Identify the cell.
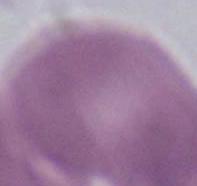
This is an erythrocyte.

Summary:
  - Magnification: 1000x
  - Modality: photomicrograph